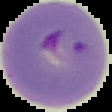

Summary:
  - Result: malaria parasites detected
  - Preparation: thin blood film
  - Image type: segmented cell region on a black background
  - Image size: 112×112 pixels